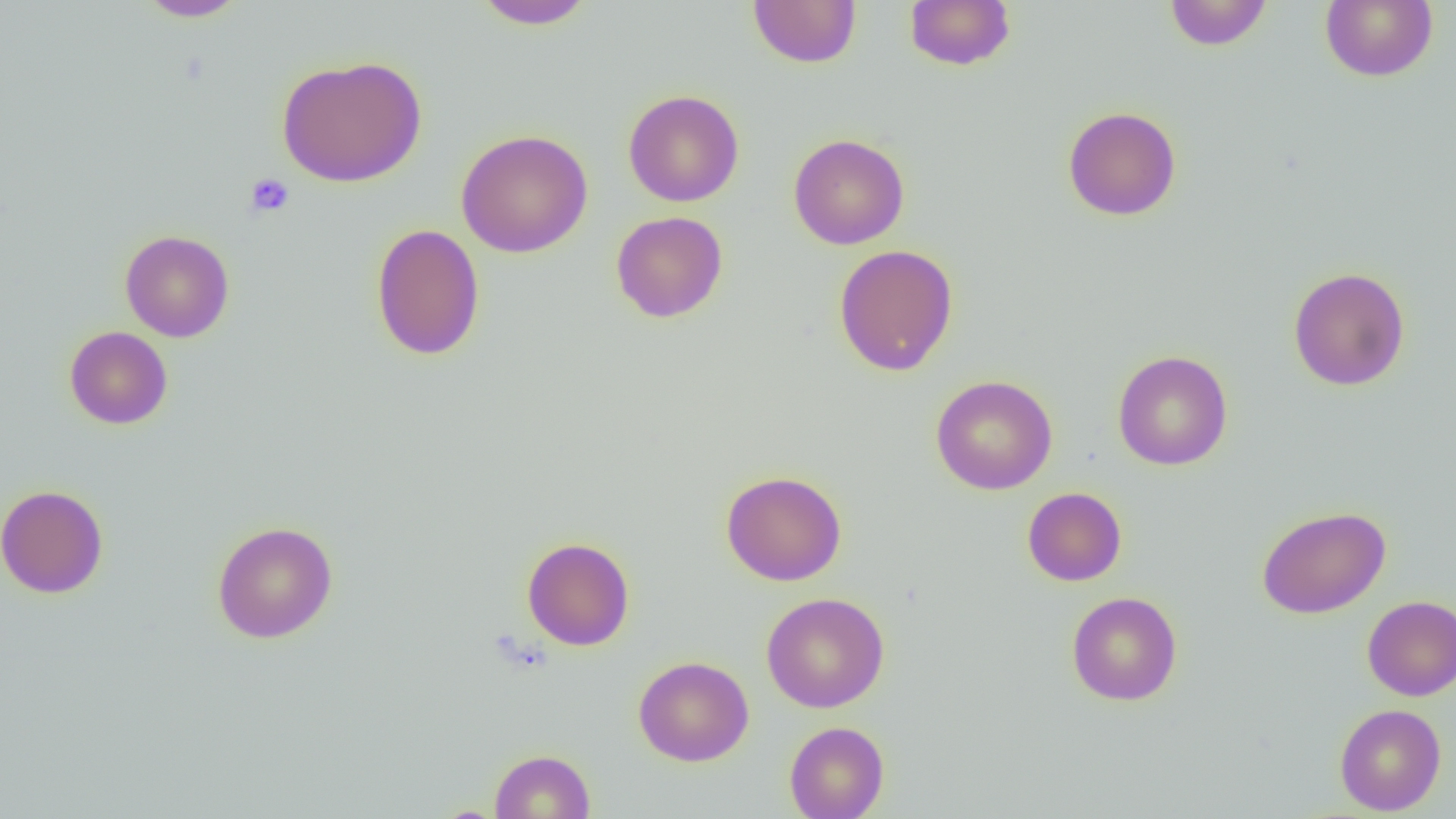

{
  "slide_level_diagnosis": "no evidence of blood parasites",
  "platelet_locations": "approximate bounding boxes as named x1/y1/x2/y2 corners in pixels: (x1=245, y1=173, x2=294, y2=218)",
  "magnification": "1000x",
  "field_of_view": "one of a larger specimen",
  "preparation": "thin blood film",
  "uninfected_red_blood_cell_locations": "approximate bounding boxes as named x1/y1/x2/y2 corners in pixels: (x1=471, y1=0, x2=598, y2=30), (x1=748, y1=0, x2=862, y2=68), (x1=904, y1=0, x2=1016, y2=71), (x1=1321, y1=0, x2=1438, y2=82), (x1=134, y1=1, x2=249, y2=21), (x1=1164, y1=1, x2=1273, y2=51), (x1=276, y1=55, x2=427, y2=187), (x1=623, y1=89, x2=744, y2=207), (x1=1062, y1=105, x2=1182, y2=221), (x1=456, y1=128, x2=593, y2=258), (x1=788, y1=133, x2=910, y2=249), (x1=610, y1=211, x2=728, y2=323), (x1=370, y1=224, x2=485, y2=361), (x1=120, y1=230, x2=234, y2=342), (x1=833, y1=244, x2=959, y2=377), (x1=1288, y1=266, x2=1410, y2=392), (x1=64, y1=326, x2=173, y2=429), (x1=1112, y1=350, x2=1233, y2=470), (x1=930, y1=374, x2=1058, y2=495), (x1=720, y1=469, x2=848, y2=586), (x1=0, y1=484, x2=109, y2=599), (x1=1022, y1=487, x2=1127, y2=586), (x1=1257, y1=505, x2=1391, y2=619), (x1=212, y1=520, x2=338, y2=644), (x1=522, y1=537, x2=635, y2=651), (x1=1066, y1=591, x2=1182, y2=706), (x1=761, y1=592, x2=890, y2=713), (x1=1361, y1=595, x2=1456, y2=701), (x1=633, y1=655, x2=754, y2=767), (x1=1334, y1=704, x2=1447, y2=815), (x1=784, y1=721, x2=889, y2=819), (x1=490, y1=749, x2=595, y2=819)",
  "image_size": "1456×819 pixels",
  "modality": "light microscopy"
}